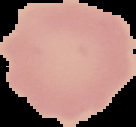

Summary:
  - Preparation: thin blood smear
  - Image size: 136×127 pixels
  - Image type: cell region segmented out of the field of view; surrounding area masked to black
  - Malaria status: uninfected